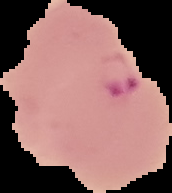
Summary:
  - Image size: 172×193 pixels
  - Preparation: thin blood smear
  - Malaria status: parasitized
  - Image type: cell region segmented out of the field of view; surrounding area masked to black